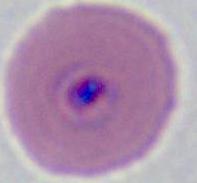
identification = Plasmodium
modality = photomicrograph
magnification = 400x or 1000x